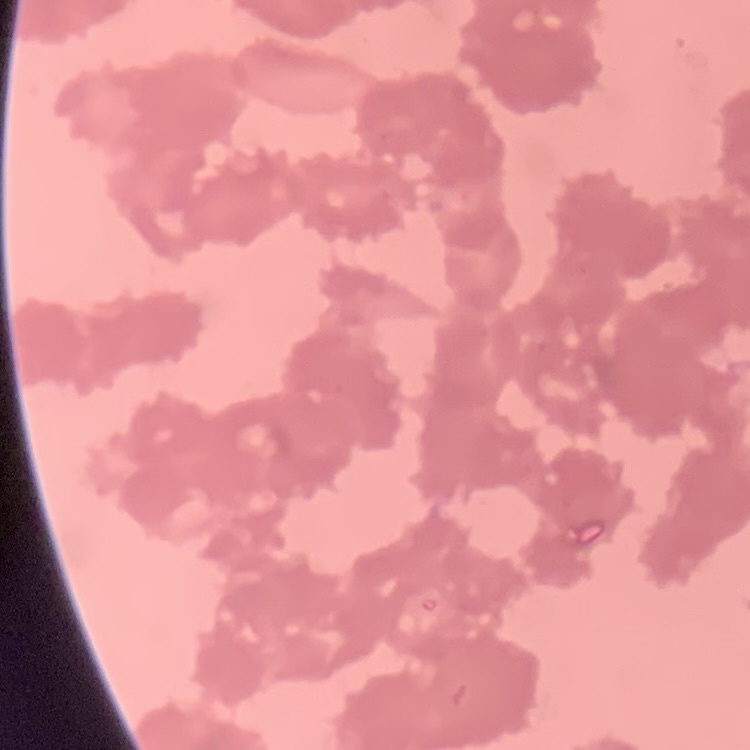
Summary:
  - Erythrocyte morphology: rouleaux formation
  - Image type: square crop of a larger photomicrograph
  - Stain: Field's or Giemsa
  - Preparation: thin peripheral smear